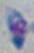
Micrograph. Toxoplasma gondii is shown. 1000x magnification.